State the preparation type.
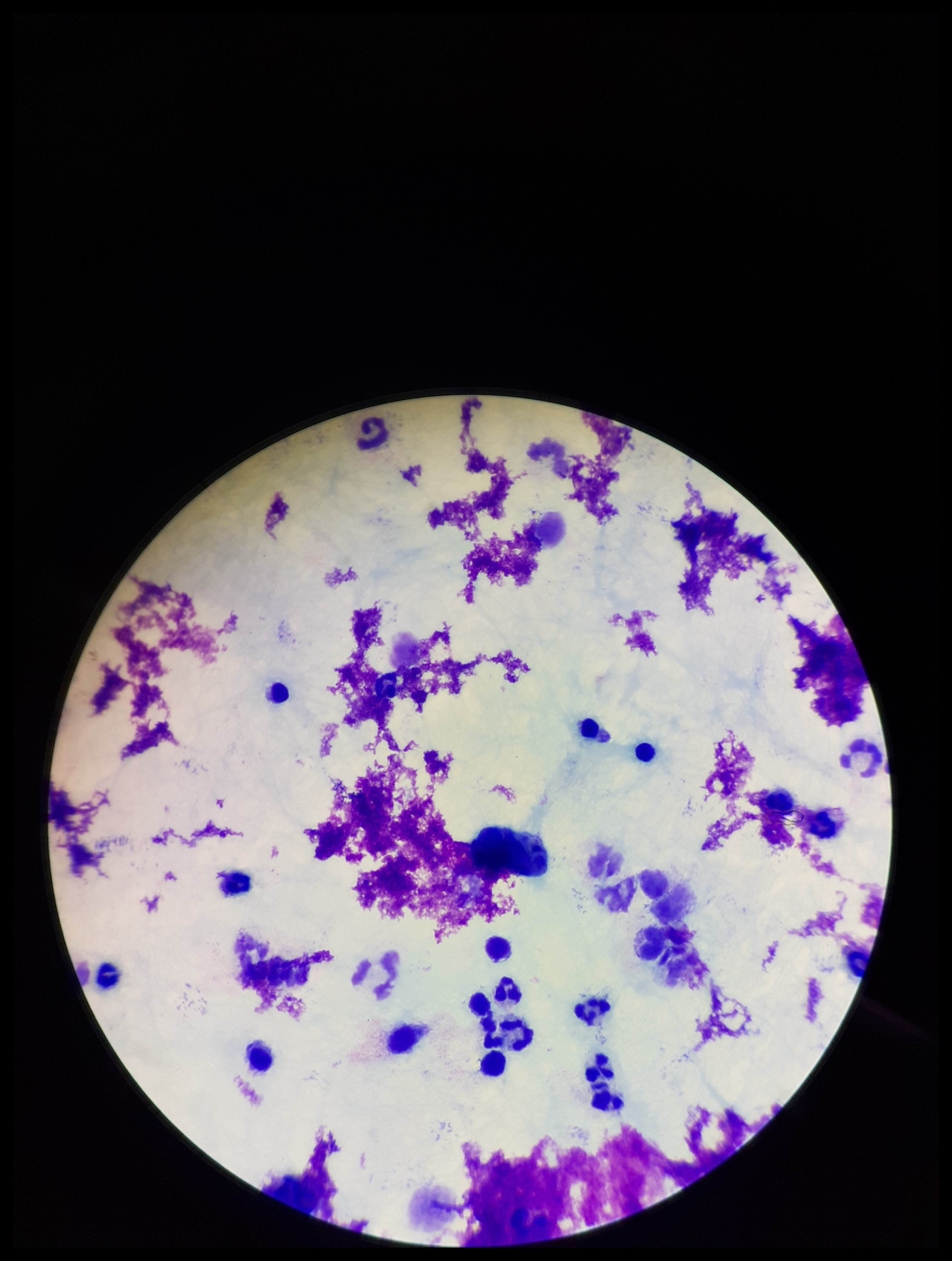

A thick smear.

Leukocyte count: 21. Plasmodium parasites: none seen. Smartphone photograph taken through the eyepiece of a microscope. Patient malaria status: negative. Parasite count: 0. Giemsa stain. One field from this slide. Image is 952×1261 pixels.